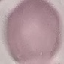
Summary:
  - Result: no malaria parasites detected
  - Capture: smartphone through the microscope eyepiece
  - Stain: Giemsa
  - Preparation: thin smear
  - Image type: cell patch, automatically extracted from a larger field of view and resized to 64 × 64 pixels